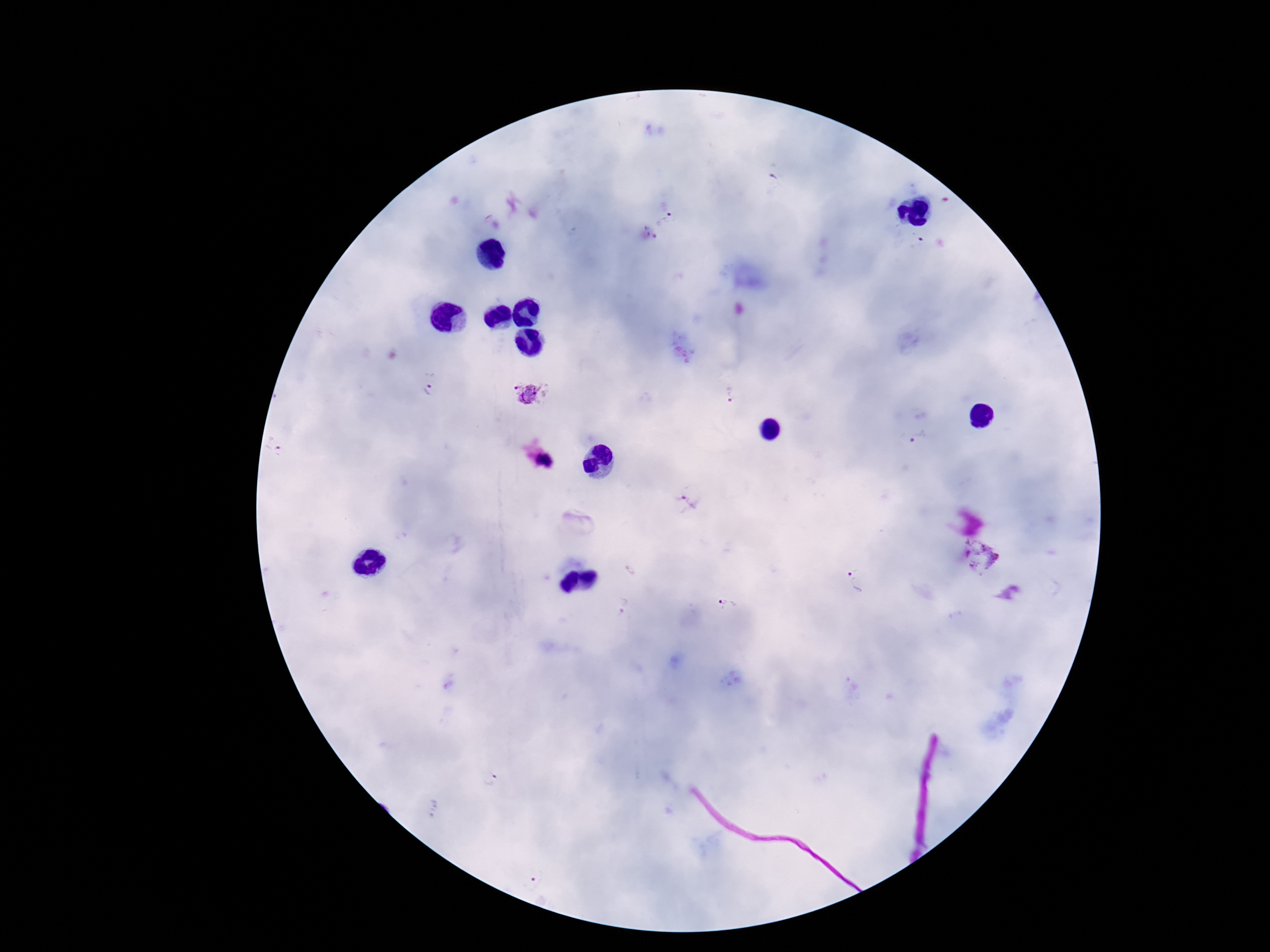
preparation = thick blood film
patient malaria status = positive
image size = 1270×952 pixels
capture = smartphone camera through the microscope eyepiece
Plasmodium parasite locations = approximate object centers, in pixels from the top-left corner: (x=668, y=221), (x=429, y=388), (x=528, y=391), (x=731, y=394), (x=921, y=438), (x=983, y=557), (x=855, y=581), (x=727, y=605)
magnification = 100x
stain = Giemsa
field of view = one from this slide